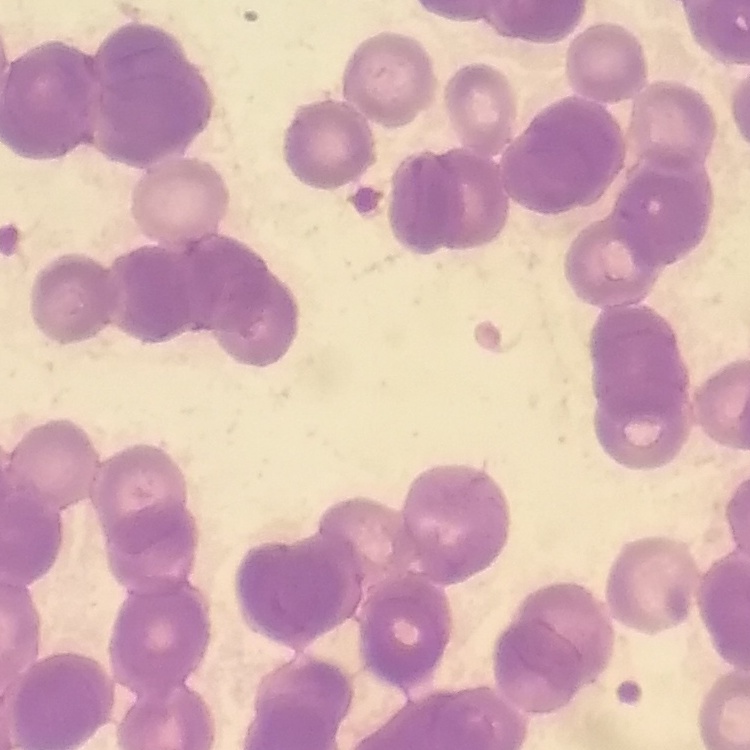
{
  "erythrocyte_morphology": "rouleaux formation",
  "image_type": "square crop of a larger photomicrograph",
  "stain": "Field's or Giemsa",
  "preparation": "thin peripheral smear"
}